Give the extent of all uninfected red blood cells.
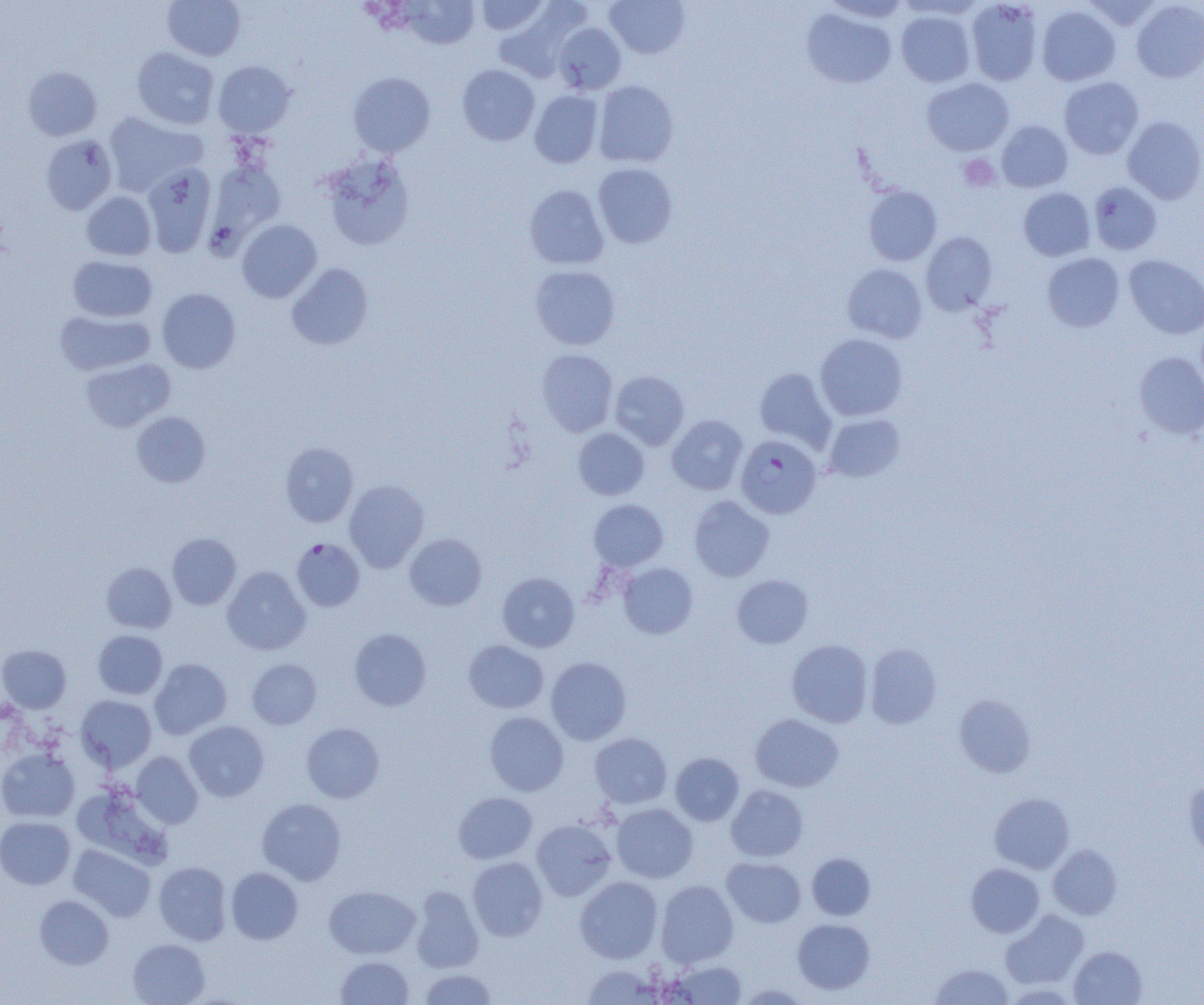
Approximate bounding boxes as (x1, y1, x2, y2) in pixels.
Uninfected red blood cells: (162, 0, 245, 60), (475, 0, 549, 35), (605, 0, 690, 59), (965, 0, 1043, 85), (1083, 0, 1161, 31), (403, 1, 480, 48), (1131, 1, 1204, 82), (494, 3, 588, 82), (1036, 5, 1121, 86), (802, 8, 897, 88), (896, 10, 975, 87), (553, 23, 626, 94), (131, 47, 219, 129), (213, 60, 296, 138), (457, 64, 540, 146), (23, 66, 102, 141), (348, 72, 436, 157), (922, 77, 1014, 156), (1059, 77, 1144, 159), (593, 80, 679, 167), (530, 90, 603, 168), (103, 112, 205, 196), (1123, 116, 1204, 204), (996, 120, 1073, 192), (40, 134, 117, 215), (320, 154, 414, 251), (207, 161, 286, 247), (592, 162, 678, 248), (141, 164, 216, 257), (1088, 182, 1162, 255), (524, 184, 609, 269), (863, 186, 941, 265), (1018, 188, 1096, 261), (81, 191, 156, 260), (237, 219, 322, 302), (921, 232, 998, 315), (1042, 253, 1125, 332), (1124, 254, 1204, 339), (67, 255, 157, 322), (286, 263, 373, 350), (842, 263, 928, 343), (529, 265, 621, 350), (157, 288, 241, 373), (55, 310, 155, 376), (815, 333, 908, 421), (536, 348, 618, 436), (1135, 352, 1204, 438), (80, 358, 175, 432), (755, 368, 836, 451), (610, 370, 689, 450), (131, 412, 210, 488), (667, 414, 748, 495), (824, 414, 905, 481), (573, 427, 649, 500), (280, 442, 359, 527), (344, 479, 429, 572), (689, 495, 774, 582), (589, 499, 668, 572), (168, 533, 241, 609), (405, 533, 487, 610), (618, 562, 698, 639), (101, 563, 176, 633), (222, 566, 310, 655), (497, 572, 580, 652), (731, 574, 814, 649), (349, 628, 431, 711), (93, 630, 167, 699), (786, 639, 873, 728), (463, 640, 549, 713), (865, 644, 942, 729), (0, 645, 71, 712), (546, 656, 632, 745), (149, 658, 231, 739), (246, 658, 322, 729), (954, 694, 1035, 777), (76, 695, 156, 771), (484, 711, 568, 796), (750, 714, 844, 792), (184, 721, 269, 801), (301, 723, 384, 803), (590, 732, 672, 808), (0, 749, 80, 822), (131, 751, 203, 828), (670, 752, 744, 826), (1184, 781, 1204, 859), (726, 785, 808, 862), (453, 792, 537, 864), (989, 792, 1075, 874), (257, 798, 346, 885), (611, 803, 698, 883), (0, 816, 75, 889), (531, 819, 616, 901), (69, 845, 155, 922), (1048, 845, 1122, 920), (807, 853, 876, 920), (468, 857, 548, 941), (722, 857, 806, 927), (154, 861, 232, 945), (966, 863, 1044, 937), (226, 867, 303, 944), (575, 876, 663, 963), (656, 880, 739, 968), (324, 885, 421, 959), (410, 887, 484, 973), (34, 895, 113, 969), (1000, 910, 1089, 989), (793, 918, 875, 994), (128, 938, 210, 1005), (1069, 945, 1147, 1005), (335, 956, 414, 1004), (666, 959, 747, 1004), (930, 963, 1014, 1004), (581, 964, 662, 1005), (418, 968, 497, 1004), (736, 982, 811, 1004).

Platelet locations: (958, 154, 1000, 192). Plasmodium falciparum-infected red blood cell locations: (736, 434, 822, 519), (292, 538, 365, 612). Slide-level diagnosis: Plasmodium falciparum. Single field of view. Image is 1204×1005 pixels. Thin blood film. Captured at 1000x magnification. Optical microscopy.